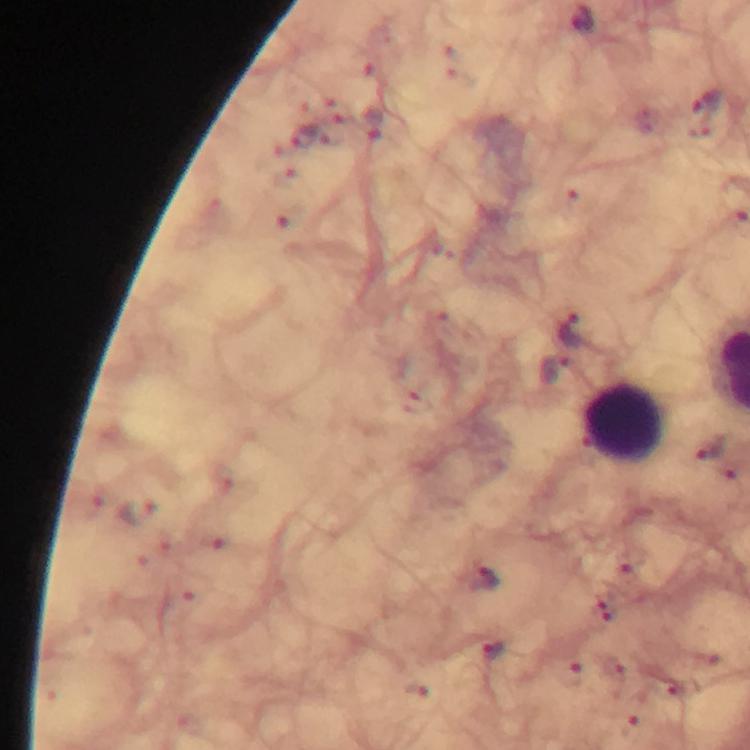
immersion oil = applied
leukocyte locations = approximate centers as [x, y] in pixels: [627, 421]
Plasmodium parasite locations = approximate centers as [x, y] in pixels: [708, 102], [575, 329], [554, 368], [711, 449], [485, 580], [493, 652]
cropped from = one field of view
magnification = 100x
image size = 750×750 pixels
capture = smartphone mounted on the microscope
context = from a diagnostic examination for malaria
preparation = thick smear
stain = Giemsa